Identify the parasite.
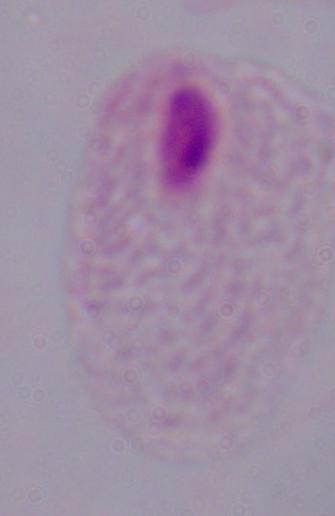
A trichomonad.

magnification: 1000x
modality: photomicrograph